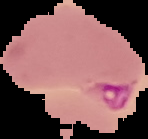 Malaria status: parasitized. Cell region segmented out of the field of view; the surrounding area is masked to black. From a thin blood smear. Image is 148×139 pixels.